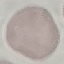
Result: no malaria parasites detected. Automatically extracted cell patch, resized to 64 × 64 pixels. Thin blood smear. Acquired by smartphone through the microscope eyepiece. Giemsa-stained preparation.